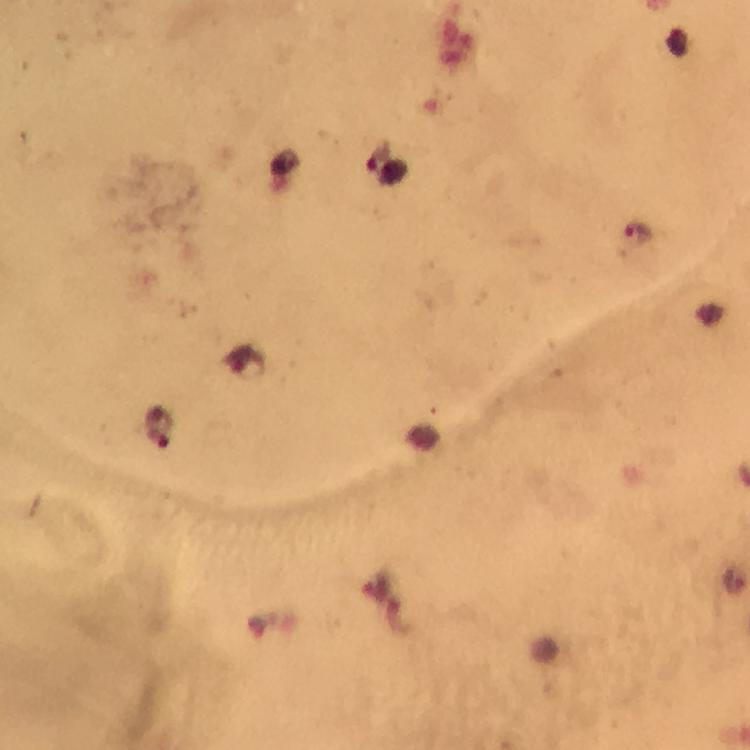
Approximate centers as (x, y) in pixels.
Summary:
  - Malaria parasite locations: (388, 172), (639, 234), (246, 364), (157, 428)
  - Context: from a malaria diagnostic workup
  - Stain: Giemsa
  - Image size: 750×750 pixels
  - Preparation: thick smear
  - Immersion oil: applied
  - Capture: smartphone mounted on the microscope
  - Magnification: 100x
  - Cropped from: a single field of view